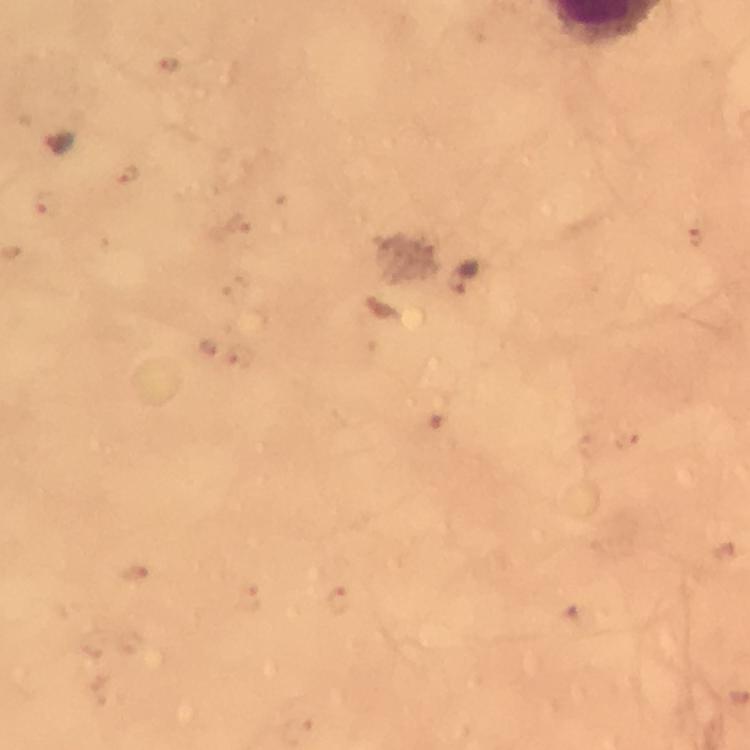
Approximate centers as {x, y} in pixels.
Summary:
  - Malaria parasite locations: {467, 276}
  - Cropped from: one field of view
  - Capture: smartphone camera through the microscope
  - Immersion oil: used
  - Magnification: 100x
  - Stain: Giemsa
  - Image size: 750×750 pixels
  - Preparation: thick blood smear
  - Context: from a diagnostic examination for malaria